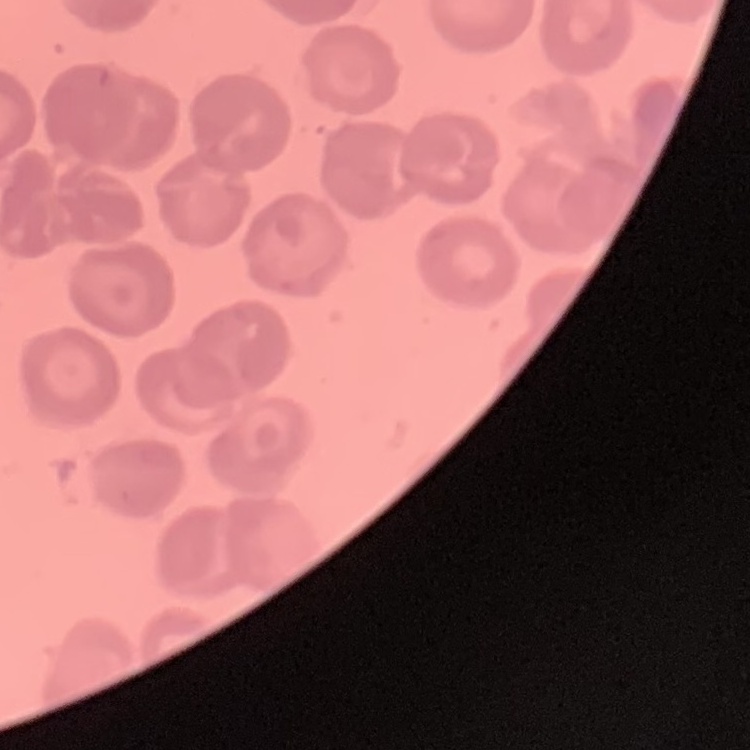

Summary:
  - Erythrocyte morphology: no rouleaux formation
  - Preparation: thin peripheral smear
  - Image type: one tile cut from a larger photomicrograph
  - Stain: Field's or Giemsa